Locate every Plasmodium malariae-infected red blood cell.
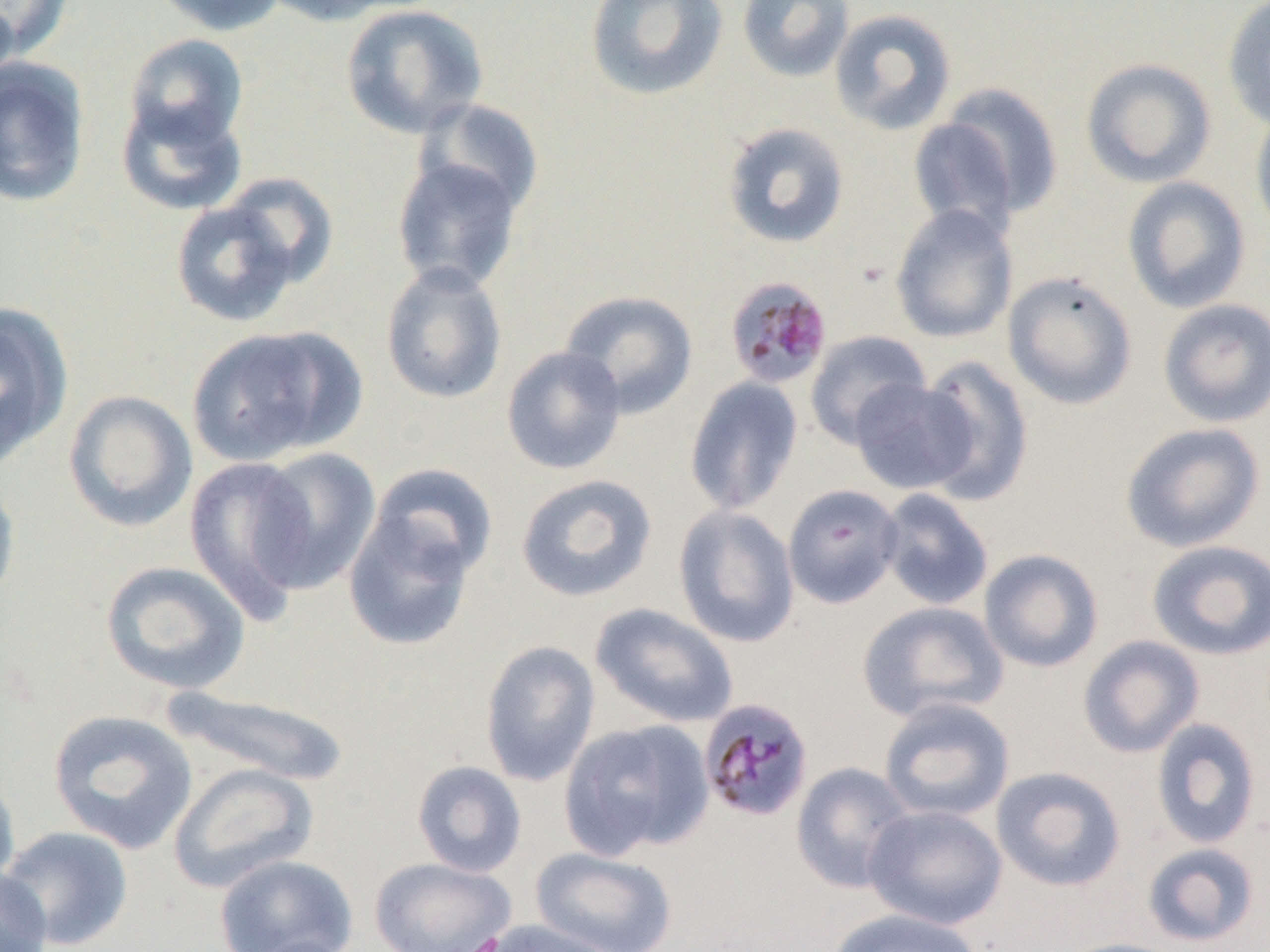
Approximate bounding boxes as (x1, y1, x2, y2) in pixels.
Plasmodium malariae-infected red blood cells: (723, 276, 833, 389), (698, 697, 814, 821).

slide_level_diagnosis: Plasmodium malariae
modality: optical microscopy
magnification: 1000x
uninfected_red_blood_cell_locations: 'approximate bounding boxes as (x1, y1, x2, y2) in pixels: (0, 0, 74, 62), (149, 0, 289, 36), (258, 0, 399, 26), (584, 0, 729, 101), (736, 0, 855, 83), (1222, 0, 1270, 133), (340, 4, 489, 139), (829, 8, 958, 136), (123, 33, 249, 154), (0, 56, 91, 207), (1080, 57, 1217, 188), (941, 82, 1065, 215), (116, 94, 249, 216), (416, 98, 544, 218), (1250, 108, 1270, 242), (907, 117, 1021, 238), (722, 122, 850, 249), (391, 155, 525, 295), (217, 172, 340, 289), (1121, 177, 1252, 314), (170, 198, 301, 328), (889, 204, 1018, 344), (380, 261, 508, 406), (1002, 271, 1137, 410), (558, 290, 699, 418), (1157, 298, 1270, 428), (0, 303, 72, 467), (185, 325, 360, 466), (805, 330, 931, 449), (501, 345, 627, 475), (915, 355, 1034, 506), (684, 376, 803, 516), (849, 378, 977, 495), (63, 390, 198, 532), (1120, 422, 1266, 553), (248, 446, 382, 594), (184, 456, 317, 619), (365, 463, 499, 583), (515, 473, 658, 602), (0, 475, 21, 609), (782, 484, 904, 608), (877, 488, 995, 612), (673, 504, 800, 648), (342, 505, 479, 653), (1146, 539, 1270, 660), (978, 548, 1104, 673), (100, 560, 251, 695), (857, 601, 1008, 723), (589, 602, 738, 729), (1077, 635, 1205, 758), (479, 640, 601, 787), (161, 686, 352, 788), (878, 697, 1016, 823), (47, 709, 198, 854), (559, 718, 714, 861), (1150, 718, 1262, 849), (411, 760, 527, 878), (167, 762, 319, 893), (790, 762, 917, 893), (990, 766, 1126, 892), (0, 768, 21, 894), (863, 804, 1008, 930), (0, 825, 134, 950), (1142, 842, 1260, 947), (532, 846, 679, 952), (213, 854, 358, 952), (369, 856, 515, 952), (0, 867, 52, 952), (826, 908, 983, 952), (469, 918, 626, 952), (237, 935, 359, 952), (1053, 937, 1189, 952)'
field_of_view: single
preparation: thin blood film
image_size: 1270×952 pixels